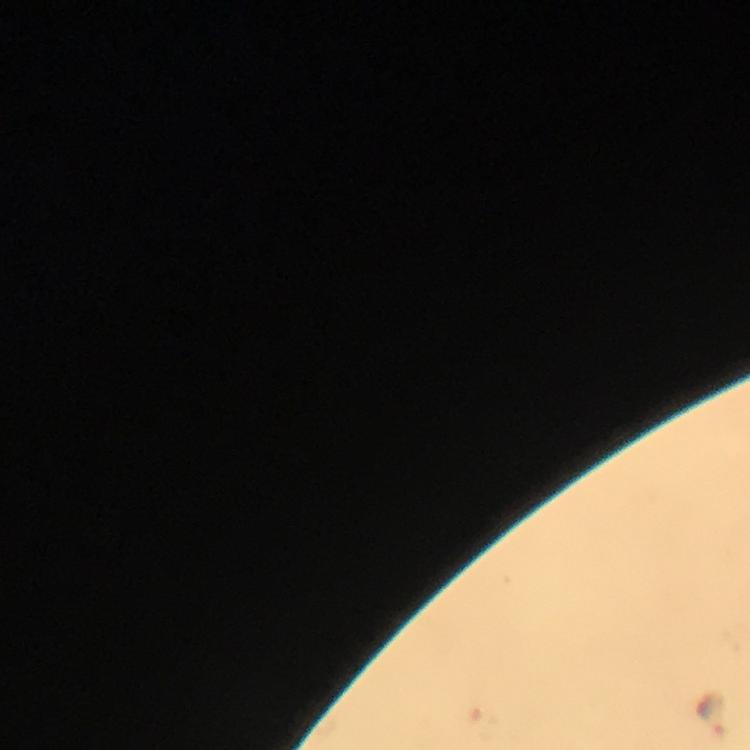 Approximate centers as (x, y) in pixels. Malaria parasite locations: (714, 715). Cropped region of a single field of view. Immersion oil was used. Thick blood smear. Image is 750×750 pixels. At 100x magnification. From a malaria diagnostic workup. Smartphone photograph taken through a microscope. Giemsa-stained preparation.